Mark where platelets are.
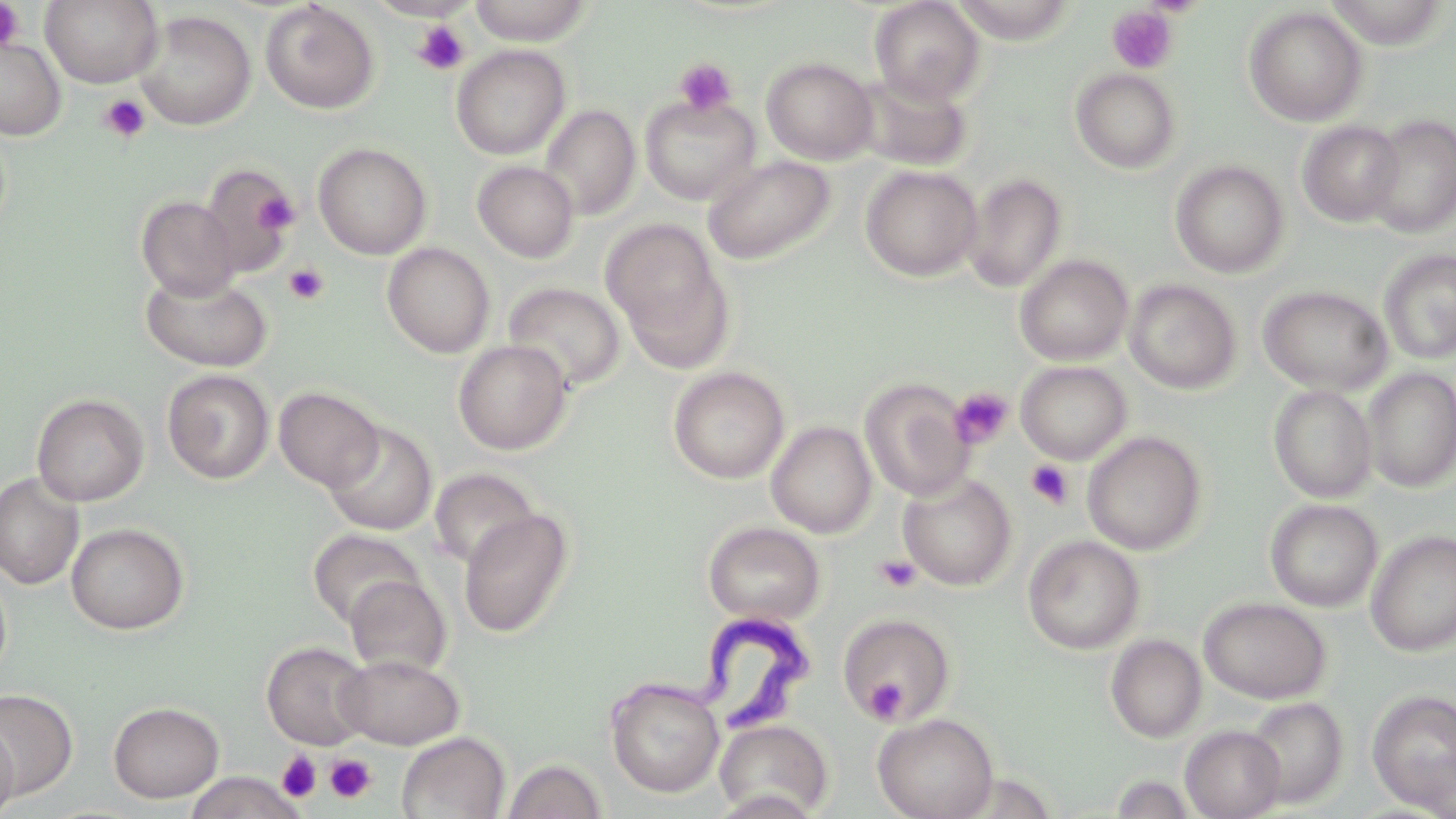
Approximate bounding boxes as (x1, y1, x2, y2) in pixels.
Platelets: (0, 1, 26, 52), (1106, 6, 1178, 74), (412, 20, 470, 75), (674, 58, 737, 116), (100, 94, 150, 143), (253, 190, 300, 235), (284, 263, 329, 305), (949, 386, 1014, 449), (1026, 460, 1074, 509), (874, 553, 922, 593), (865, 677, 908, 722), (277, 752, 321, 802), (325, 753, 377, 803).

Trypanosoma brucei locations: (611, 612, 819, 751). Uninfected red blood cell locations: (41, 0, 162, 88), (468, 0, 595, 45), (869, 0, 986, 106), (260, 2, 380, 114), (1243, 6, 1368, 126), (134, 10, 256, 131), (0, 38, 66, 140), (451, 44, 570, 160), (761, 56, 879, 165), (1070, 68, 1181, 174), (852, 70, 973, 172), (639, 94, 760, 205), (539, 103, 640, 220), (1364, 115, 1456, 238), (1297, 120, 1405, 227), (313, 142, 432, 260), (703, 155, 835, 265), (1170, 159, 1289, 278), (472, 161, 579, 262), (199, 164, 300, 277), (860, 165, 982, 281), (962, 172, 1068, 293), (136, 196, 240, 300), (603, 220, 733, 369), (382, 242, 495, 358), (1378, 249, 1456, 364), (1014, 255, 1134, 365), (140, 272, 272, 371), (1124, 280, 1241, 394), (503, 282, 627, 391), (1258, 285, 1392, 395), (452, 340, 573, 455), (1015, 361, 1132, 464), (668, 366, 789, 484), (1361, 367, 1456, 493), (162, 369, 275, 484), (859, 377, 975, 501), (1268, 384, 1377, 502), (274, 386, 384, 491), (31, 393, 149, 506), (322, 421, 437, 536), (766, 421, 877, 538), (1082, 431, 1209, 555), (430, 467, 541, 571), (0, 472, 84, 590), (898, 472, 1017, 590), (1265, 498, 1383, 612), (458, 510, 574, 637), (703, 521, 825, 625), (66, 523, 189, 634), (308, 528, 424, 628), (1365, 530, 1456, 656), (1023, 535, 1145, 654), (0, 569, 11, 683), (345, 575, 452, 676), (1199, 597, 1332, 703), (838, 613, 956, 723), (1105, 634, 1207, 743), (262, 641, 373, 749), (335, 653, 465, 749), (606, 677, 724, 798), (1, 688, 79, 798), (1367, 689, 1456, 813), (1244, 696, 1348, 808), (108, 700, 225, 803), (872, 712, 998, 819), (713, 718, 834, 818), (0, 719, 20, 819), (1180, 725, 1286, 819), (397, 731, 510, 819), (502, 758, 608, 819), (184, 771, 306, 818). Slide-level diagnosis: Trypanosoma brucei. Image is 1456×819 pixels. Thin blood smear. Captured at 1000x magnification. Light microscopy. May-Grünwald-Giemsa stain. One field of a larger specimen.